Outline platelets.
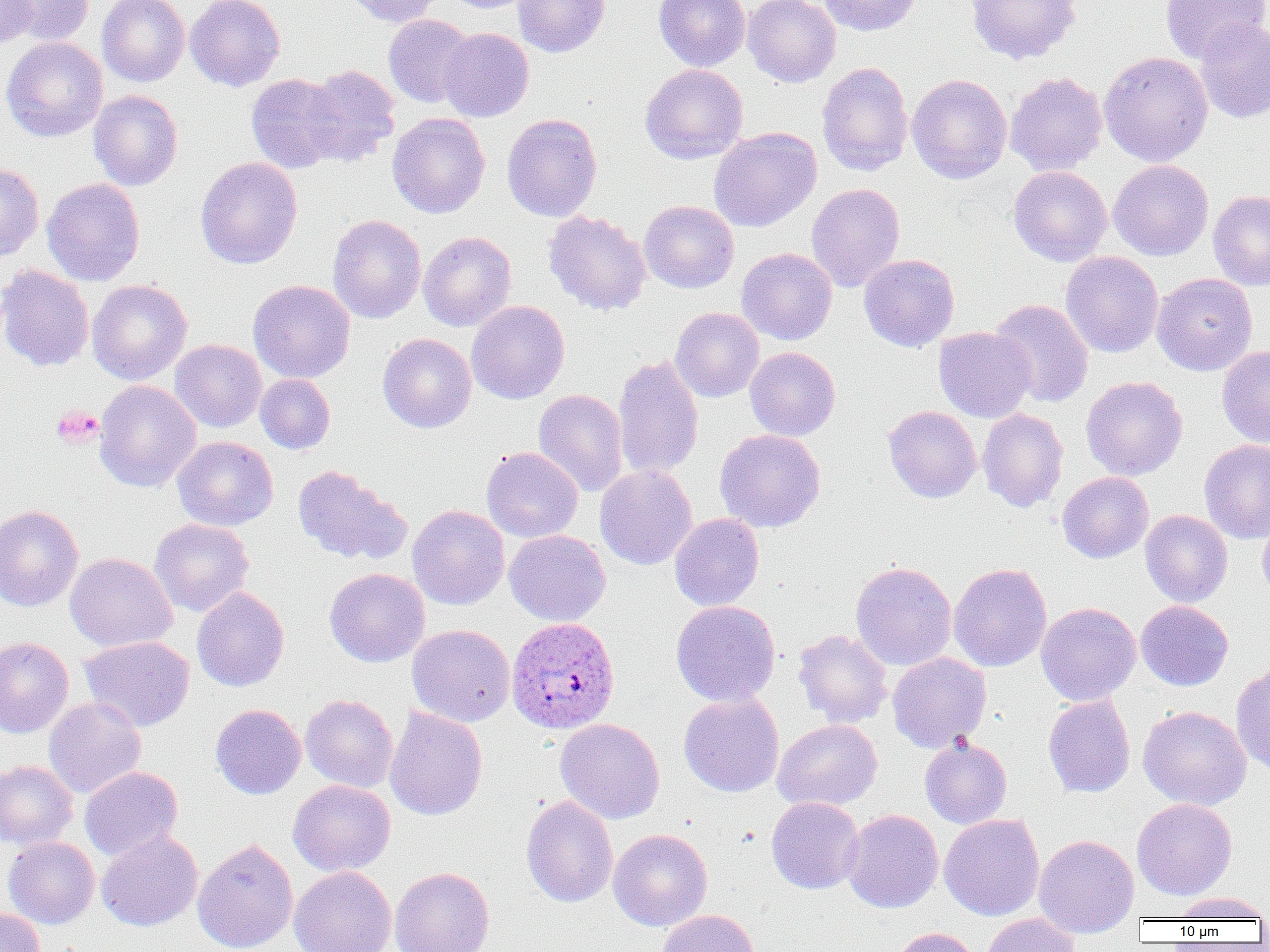
Approximate bounding boxes as [x1, y1, x2, y2] in pixels.
Platelets: [50, 405, 103, 450].

Uninfected red blood cell locations: [0, 0, 40, 48], [7, 0, 94, 46], [97, 0, 190, 87], [185, 0, 285, 91], [345, 0, 444, 27], [442, 0, 537, 13], [513, 0, 609, 57], [654, 0, 750, 71], [743, 0, 840, 87], [816, 0, 923, 36], [965, 0, 1081, 65], [1160, 0, 1269, 63], [383, 14, 477, 108], [1194, 19, 1270, 123], [439, 27, 534, 122], [0, 37, 108, 142], [1099, 51, 1214, 166], [816, 61, 914, 176], [640, 64, 748, 164], [302, 65, 400, 165], [1005, 71, 1108, 176], [246, 73, 347, 173], [907, 74, 1012, 184], [89, 90, 183, 191], [387, 112, 490, 218], [502, 113, 602, 222], [709, 127, 821, 232], [195, 156, 303, 269], [1108, 160, 1213, 261], [0, 162, 44, 262], [1008, 165, 1112, 266], [42, 178, 144, 286], [806, 183, 905, 291], [1208, 189, 1270, 290], [639, 200, 739, 294], [543, 210, 652, 315], [327, 214, 426, 323], [418, 231, 516, 331], [736, 247, 837, 346], [1060, 251, 1163, 358], [859, 254, 959, 352], [0, 264, 94, 372], [1151, 272, 1257, 376], [87, 279, 192, 385], [248, 279, 356, 384], [989, 298, 1094, 408], [466, 300, 569, 404], [670, 307, 764, 402], [934, 327, 1036, 422], [377, 333, 477, 433], [170, 339, 267, 432], [1217, 344, 1270, 448], [745, 347, 840, 441], [612, 354, 704, 480], [255, 374, 335, 454], [1080, 376, 1188, 481], [94, 380, 201, 492], [533, 389, 629, 497], [883, 405, 982, 503], [977, 408, 1069, 512], [714, 429, 826, 533], [172, 436, 278, 530], [1199, 439, 1270, 544], [481, 446, 583, 542], [291, 465, 411, 565], [595, 465, 697, 569], [1057, 471, 1154, 563], [0, 505, 84, 611], [407, 505, 509, 610], [1140, 510, 1233, 607], [669, 513, 765, 611], [1257, 515, 1270, 601], [149, 518, 254, 617], [504, 529, 611, 626], [65, 552, 177, 651], [850, 560, 957, 670], [948, 563, 1052, 672], [324, 568, 430, 667], [192, 586, 290, 692], [671, 600, 781, 707], [1135, 600, 1234, 691], [1036, 602, 1141, 706], [407, 624, 515, 727], [793, 629, 893, 728], [78, 635, 195, 731], [0, 637, 74, 738], [887, 652, 991, 752], [1231, 664, 1270, 775], [678, 693, 784, 797], [300, 694, 398, 793], [1042, 695, 1135, 798], [43, 697, 146, 798], [210, 704, 307, 799], [1138, 705, 1251, 811], [384, 706, 487, 821], [555, 718, 665, 824], [772, 719, 883, 811], [919, 736, 1012, 829], [0, 760, 78, 850], [80, 766, 182, 860], [288, 779, 396, 877], [520, 794, 618, 908], [766, 796, 864, 894], [1132, 797, 1237, 900], [841, 809, 944, 913], [939, 813, 1045, 920], [608, 828, 712, 931], [96, 829, 203, 931], [1034, 834, 1139, 938], [3, 836, 100, 929], [192, 837, 298, 952], [289, 866, 397, 952], [390, 866, 495, 952], [1173, 892, 1268, 921], [0, 906, 45, 952], [656, 909, 760, 952], [981, 913, 1080, 952], [888, 927, 981, 952]. Plasmodium ovale-infected red blood cell locations: [506, 616, 619, 733]. Slide-level diagnosis: Plasmodium ovale. Optical microscopy. Captured at 1000x magnification. Single field of view. Image is 1270×952 pixels. Thin blood smear.